Outline each blood parasite and name the species.
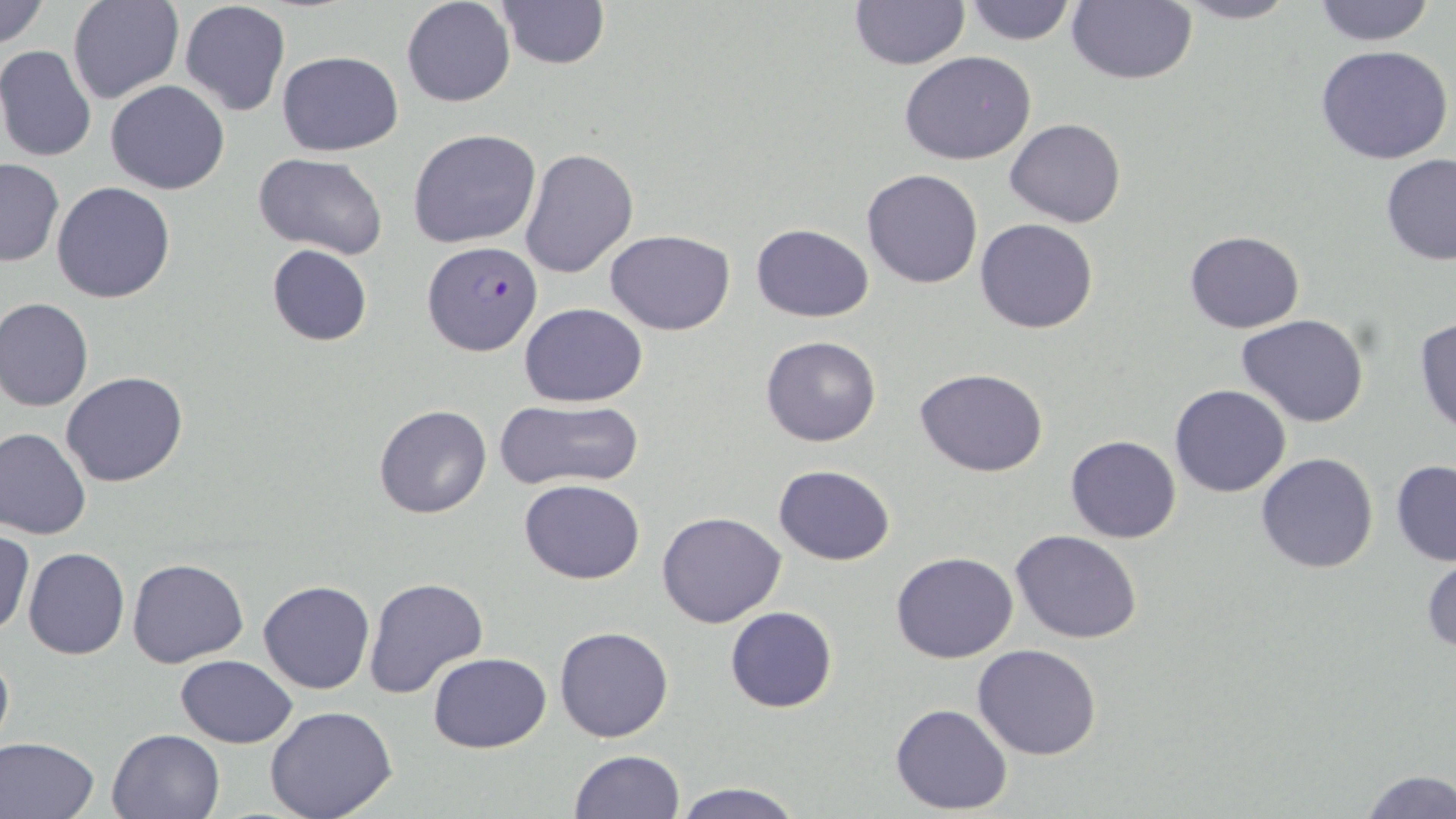

Approximate bounding boxes as [x1, y1, x2, y2] in pixels.
Plasmodium falciparum-infected red blood cells: [422, 240, 543, 357].
No Plasmodium ovale, Plasmodium malariae, Plasmodium vivax, Babesia divergens, or Trypanosoma brucei observed.

Summary:
  - Uninfected red blood cell locations: [0, 0, 49, 48], [68, 0, 183, 104], [179, 0, 292, 117], [494, 0, 610, 71], [961, 0, 1076, 46], [1067, 0, 1198, 86], [1167, 0, 1301, 24], [401, 1, 515, 108], [848, 1, 969, 70], [1308, 1, 1439, 46], [0, 45, 98, 164], [1315, 45, 1456, 166], [277, 51, 402, 156], [899, 52, 1038, 164], [104, 79, 230, 195], [1005, 118, 1125, 227], [408, 128, 541, 248], [519, 147, 638, 280], [253, 152, 388, 258], [1380, 154, 1456, 266], [1, 159, 64, 267], [861, 169, 983, 289], [52, 181, 176, 303], [975, 218, 1100, 334], [751, 223, 874, 321], [606, 230, 735, 335], [1183, 231, 1304, 333], [266, 245, 373, 346], [0, 297, 94, 412], [519, 301, 647, 407], [1236, 314, 1369, 426], [1414, 316, 1456, 438], [761, 335, 881, 448], [915, 368, 1050, 478], [61, 370, 188, 487], [1170, 384, 1290, 498], [493, 399, 644, 490], [373, 404, 492, 518], [0, 426, 92, 539], [1065, 434, 1181, 543], [1255, 453, 1380, 574], [1391, 459, 1456, 566], [772, 464, 895, 565], [519, 480, 647, 584], [658, 510, 786, 627], [1, 529, 34, 638], [1012, 530, 1143, 643], [24, 548, 129, 660], [890, 551, 1018, 662], [1421, 551, 1455, 657], [128, 558, 249, 667], [364, 576, 488, 698], [258, 579, 375, 695], [724, 607, 838, 713], [553, 626, 674, 743], [0, 644, 14, 757], [972, 644, 1102, 759], [428, 652, 551, 753], [175, 654, 298, 747], [891, 703, 1012, 814], [264, 705, 399, 819], [107, 728, 224, 818], [0, 736, 101, 819], [570, 749, 686, 818], [1358, 769, 1455, 819], [670, 780, 805, 819]
  - Slide-level diagnosis: Plasmodium falciparum
  - Modality: light microscopy
  - Stain: May-Grünwald-Giemsa
  - Magnification: 1000x
  - Image size: 1456×819 pixels
  - Field of view: one of a larger specimen
  - Preparation: thin blood film